Locate and identify every blood parasite.
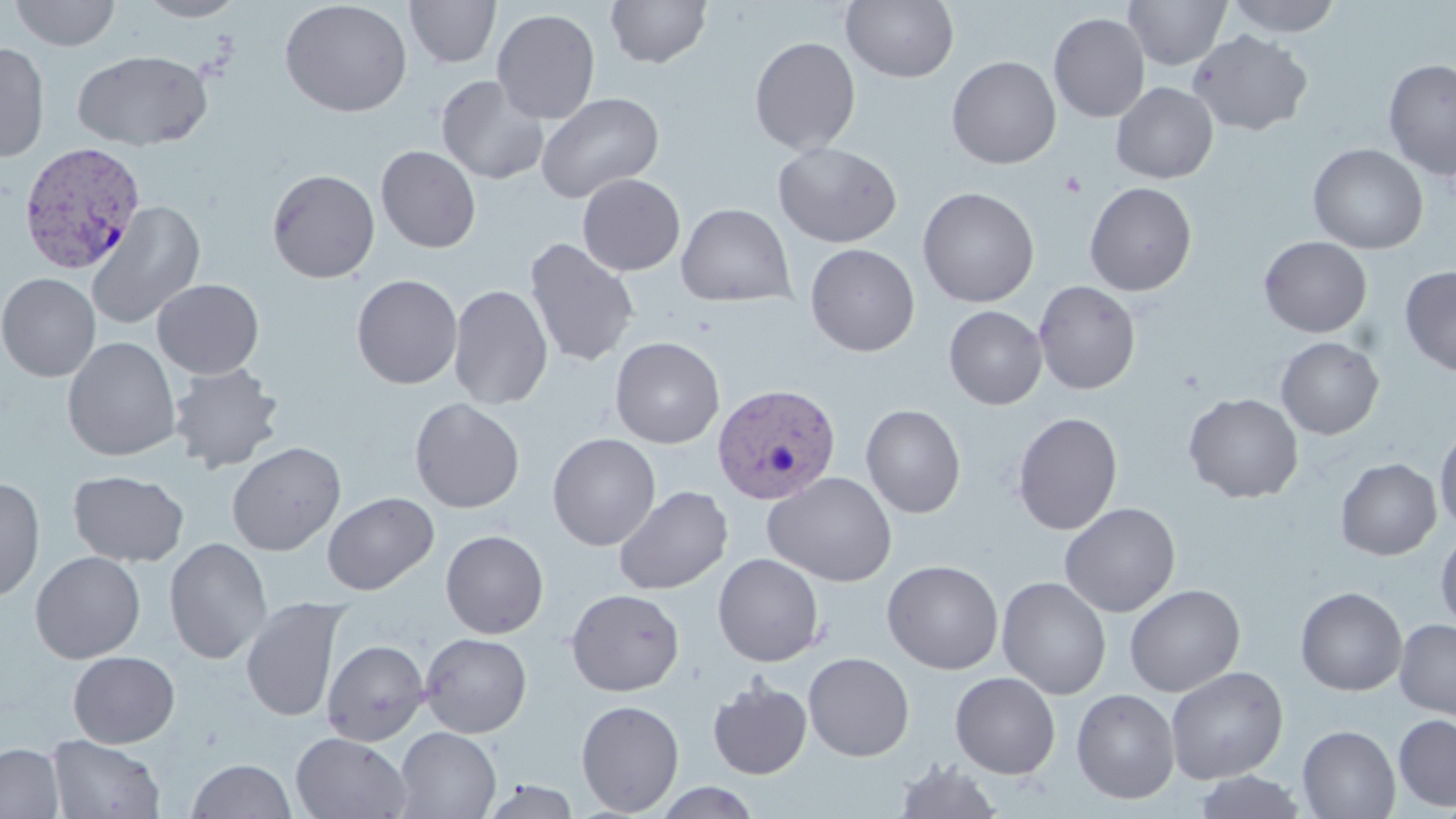

Approximate bounding boxes as (x1, y1, x2, y2) in pixels.
Plasmodium vivax-infected red blood cells: (19, 141, 147, 274), (711, 383, 842, 505).
No Plasmodium falciparum, Plasmodium ovale, Plasmodium malariae, Babesia divergens, or Trypanosoma brucei observed.

Uninfected red blood cell locations: (9, 0, 122, 50), (134, 0, 248, 21), (279, 0, 412, 118), (404, 0, 501, 68), (604, 0, 713, 68), (841, 0, 959, 83), (1123, 0, 1231, 70), (1224, 0, 1344, 37), (492, 8, 601, 124), (1048, 12, 1149, 122), (1187, 29, 1313, 136), (749, 36, 861, 155), (0, 41, 50, 162), (72, 49, 212, 150), (946, 56, 1062, 169), (1382, 58, 1455, 180), (435, 74, 549, 185), (1111, 82, 1218, 184), (536, 91, 664, 204), (773, 142, 902, 248), (1307, 143, 1428, 254), (376, 145, 481, 253), (266, 169, 380, 283), (577, 173, 685, 276), (1084, 182, 1197, 296), (917, 187, 1039, 307), (86, 201, 205, 329), (675, 203, 795, 307), (1258, 236, 1372, 337), (522, 237, 640, 367), (805, 243, 920, 356), (1399, 265, 1456, 376), (0, 272, 101, 382), (351, 274, 463, 389), (152, 278, 264, 379), (1033, 280, 1141, 395), (448, 285, 552, 410), (943, 305, 1047, 409), (610, 336, 725, 448), (1275, 336, 1384, 439), (62, 337, 181, 461), (168, 363, 284, 475), (1184, 392, 1304, 503), (409, 398, 525, 513), (861, 404, 966, 519), (1012, 412, 1123, 535), (1434, 425, 1456, 533), (548, 432, 661, 551), (227, 442, 346, 556), (1335, 458, 1441, 560), (68, 470, 189, 566), (763, 472, 897, 587), (0, 476, 45, 601), (614, 485, 733, 595), (323, 492, 439, 595), (1059, 502, 1180, 617), (1435, 528, 1456, 633), (440, 529, 549, 639), (164, 537, 272, 664), (30, 551, 146, 663), (713, 553, 825, 667), (882, 560, 1004, 673), (997, 576, 1111, 699), (1124, 584, 1245, 697), (1295, 587, 1408, 696), (565, 588, 685, 695), (240, 597, 348, 722), (1395, 619, 1456, 719), (419, 633, 532, 738), (322, 639, 430, 746), (67, 651, 180, 748), (803, 652, 915, 761), (1165, 666, 1288, 784), (949, 671, 1061, 779), (708, 677, 812, 779), (1071, 688, 1180, 804), (576, 699, 684, 816), (1393, 714, 1456, 811), (1297, 725, 1400, 819), (394, 727, 502, 819), (291, 732, 412, 818), (47, 734, 165, 818), (0, 743, 64, 819), (187, 758, 296, 818), (892, 758, 1004, 819), (1192, 770, 1307, 818), (478, 780, 583, 819), (651, 782, 762, 818). Platelet locations: (1059, 171, 1086, 197). Slide-level diagnosis: Plasmodium vivax. Thin blood film. Image is 1456×819 pixels. One field of a larger specimen. Captured at 1000x magnification. May-Grünwald-Giemsa-stained preparation. Light microscopy.